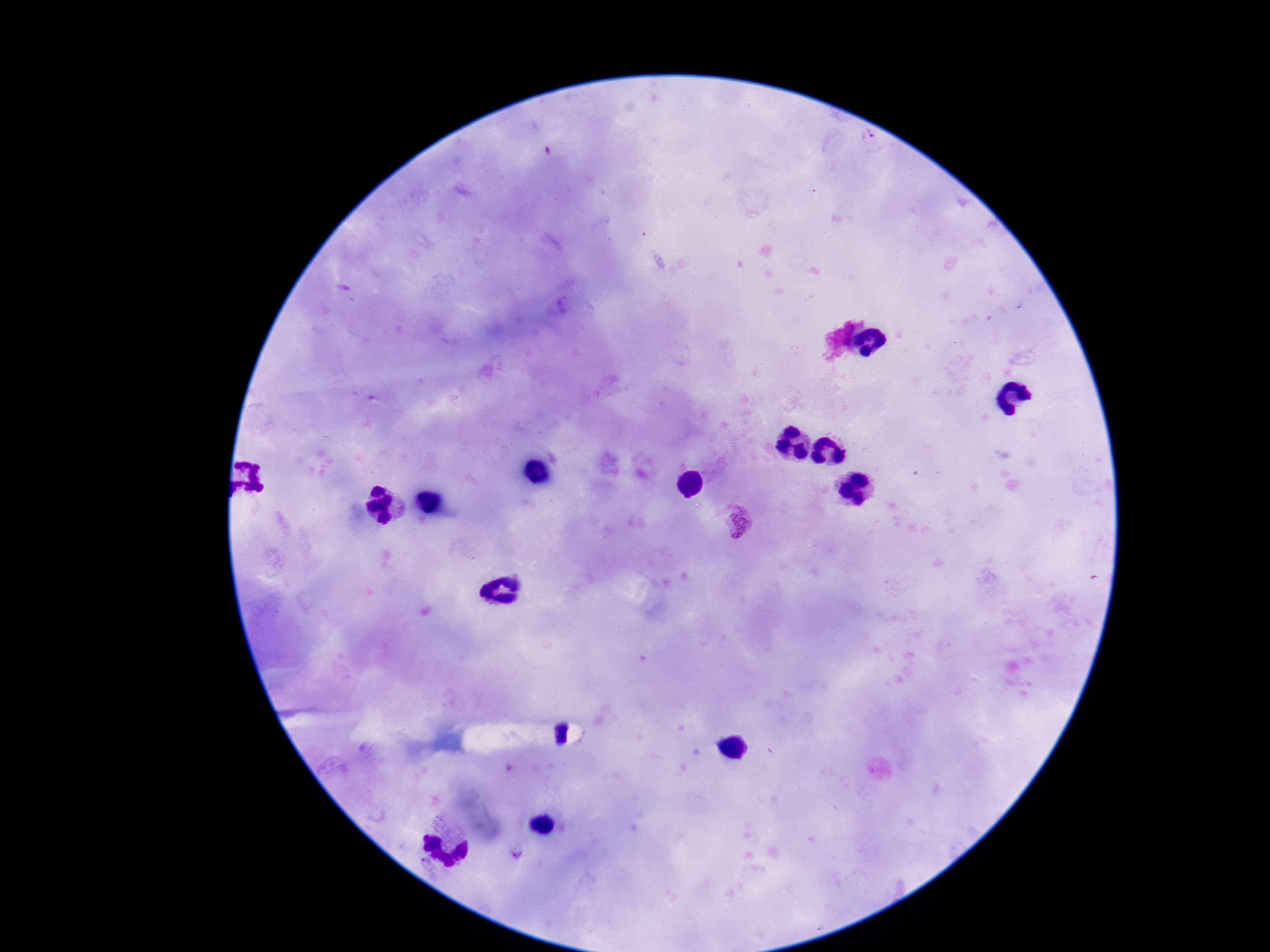
stain: Giemsa
patient_malaria_status: infected
plasmodium_parasite_locations: 'approximate centers as (x, y) in pixels: (734, 520)'
preparation: thick peripheral-blood smear
field_of_view: single
image_size: 1270×952 pixels
magnification: 100x
capture: smartphone camera through the microscope eyepiece